Assess this cell for malaria.
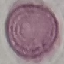

It is uninfected.

Photographed with a smartphone camera at the microscope eyepiece. Giemsa stain. Thin blood smear. Cell patch, automatically extracted from a larger field of view and resized to 64 × 64 pixels.